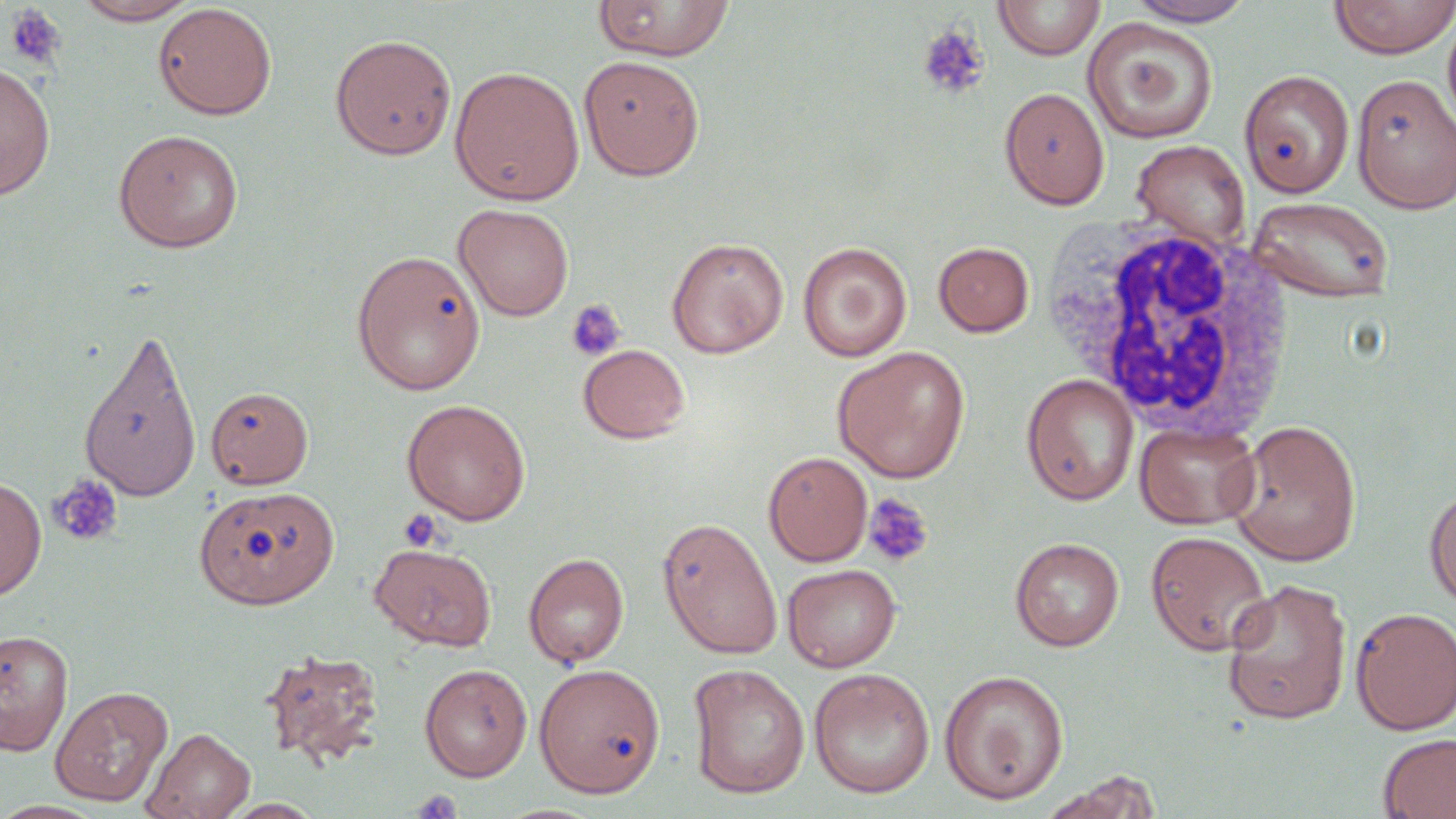

Summary:
  - Coordinate format: approximate bounding boxes as (x1,y1)-(x2,y2) corner pairs in pixels
  - Platelet locations: (4,4)-(68,69), (916,26)-(990,101), (565,300)-(627,362), (47,473)-(123,547), (862,492)-(934,568), (398,508)-(444,553), (410,789)-(464,819)
  - White blood cell locations: (1047,221)-(1295,442)
  - Uninfected red blood cell locations: (71,0)-(201,25), (593,0)-(736,61), (1127,0)-(1257,26), (1327,0)-(1456,59), (991,1)-(1106,61), (153,3)-(277,120), (1442,10)-(1456,138), (1082,16)-(1218,144), (330,33)-(457,161), (578,54)-(705,181), (0,61)-(56,200), (449,66)-(585,205), (1240,69)-(1354,198), (1351,73)-(1456,214), (999,87)-(1109,210), (113,128)-(244,253), (1131,139)-(1251,248), (1248,196)-(1395,303), (454,203)-(574,321), (667,237)-(789,358), (798,242)-(912,362), (933,242)-(1034,336), (351,249)-(485,394), (78,326)-(203,502), (578,344)-(691,444), (832,346)-(971,483), (1021,373)-(1139,506), (206,386)-(313,489), (402,399)-(530,525), (1227,419)-(1362,566), (1135,421)-(1261,530), (763,451)-(872,566), (0,477)-(46,600), (195,486)-(339,610), (1424,486)-(1456,611), (657,516)-(782,660), (1145,531)-(1272,656), (1010,536)-(1124,651), (369,542)-(497,651), (523,553)-(629,668), (782,563)-(901,672), (1220,578)-(1352,725), (1350,606)-(1456,735), (0,629)-(74,756), (258,646)-(386,770), (419,663)-(532,782), (534,663)-(666,799), (687,663)-(811,799), (809,668)-(934,799), (939,668)-(1069,805), (50,686)-(173,807), (143,726)-(256,819), (1378,732)-(1456,819), (1040,771)-(1165,819), (217,799)-(327,818)
  - Slide-level diagnosis: no evidence of blood parasites
  - Image size: 1456×819 pixels
  - Field of view: one of a larger specimen
  - Stain: May-Grünwald-Giemsa
  - Magnification: 1000x
  - Modality: light microscopy
  - Preparation: thin blood smear